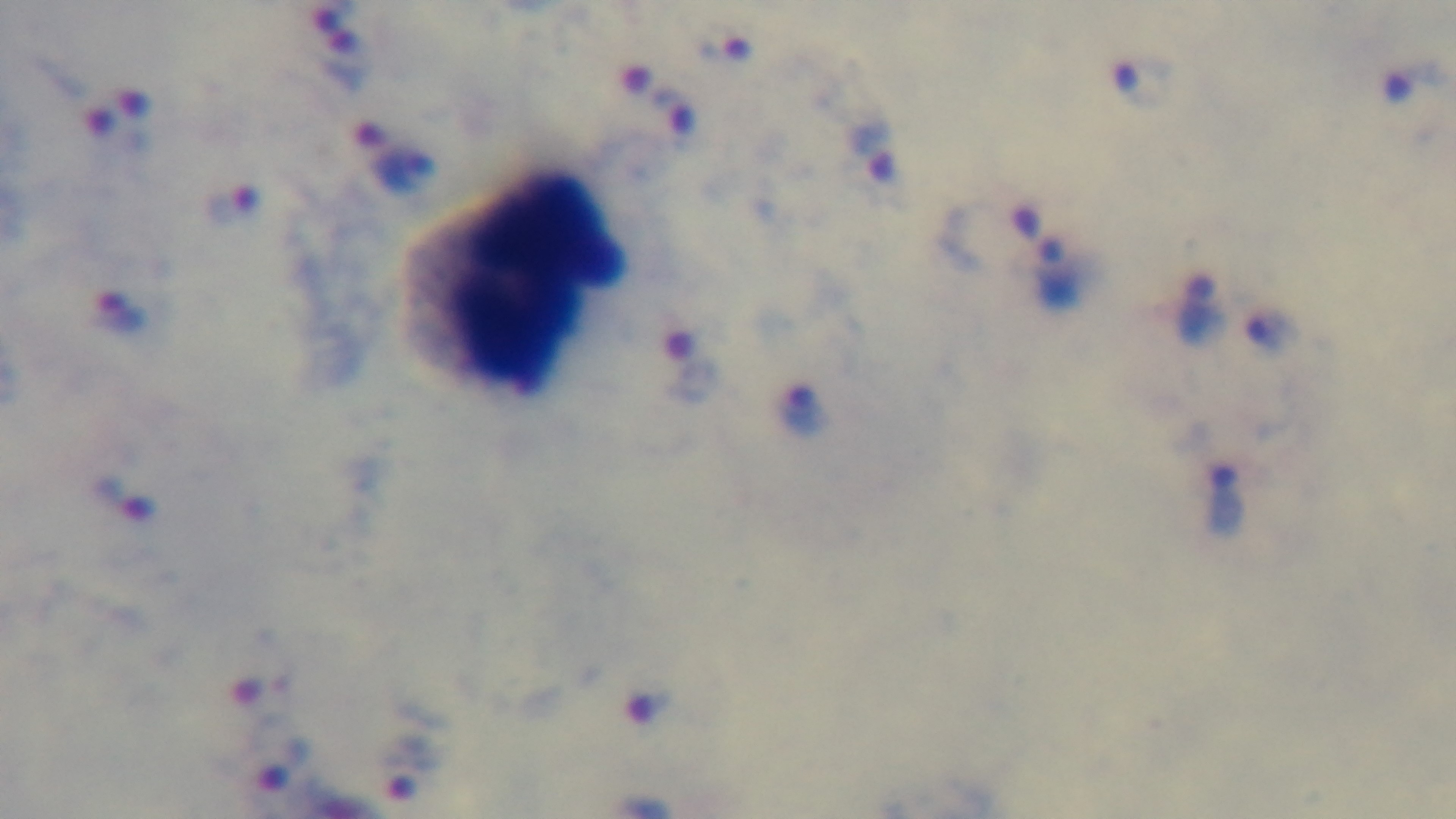

Single field of view. Giemsa-stained. Preparation: thick blood film. Light microscopy. Mounted 4K digital camera. Malaria status: positive. 100x oil-immersion objective.